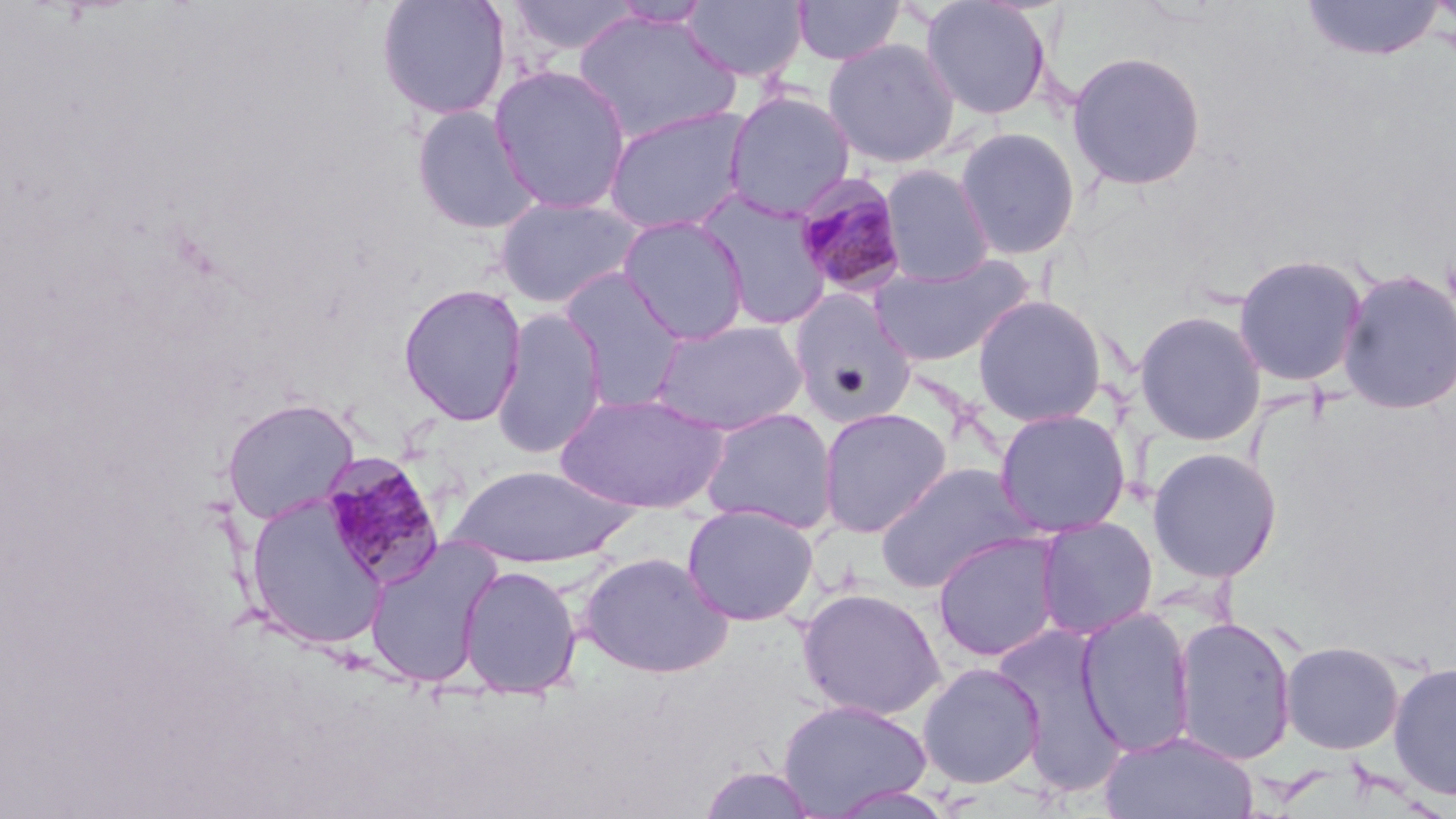

slide-level diagnosis = Plasmodium malariae
preparation = thin blood smear
magnification = 1000x
uninfected red blood cell locations = approximate bounding boxes as (x1, y1, x2, y2) in pixels: (375, 0, 510, 121), (505, 0, 644, 57), (792, 0, 906, 65), (918, 0, 1053, 121), (607, 1, 714, 29), (682, 1, 810, 84), (1300, 1, 1448, 62), (573, 10, 740, 146), (822, 37, 960, 169), (1067, 50, 1207, 191), (489, 64, 632, 214), (723, 90, 857, 219), (603, 105, 754, 235), (410, 106, 543, 235), (953, 126, 1082, 261), (879, 164, 996, 286), (694, 188, 835, 330), (493, 195, 645, 309), (616, 214, 751, 345), (868, 251, 1036, 367), (1233, 252, 1369, 387), (558, 267, 690, 412), (1337, 267, 1456, 415), (398, 283, 527, 426), (787, 290, 918, 426), (971, 293, 1109, 427), (490, 309, 609, 460), (1132, 309, 1267, 446), (648, 319, 810, 435), (554, 390, 729, 514), (221, 398, 359, 525), (817, 406, 952, 538), (698, 407, 840, 535), (993, 408, 1132, 538), (1146, 447, 1282, 583), (873, 462, 1036, 593), (446, 465, 637, 569), (245, 494, 387, 650), (681, 502, 820, 626), (1035, 515, 1158, 640), (932, 531, 1065, 662), (364, 537, 501, 688), (578, 551, 733, 679), (458, 565, 582, 697), (797, 587, 946, 720), (1077, 606, 1195, 756), (1172, 614, 1298, 765), (991, 622, 1129, 795), (1280, 640, 1405, 754), (1387, 661, 1456, 802), (916, 662, 1046, 789), (778, 697, 932, 817), (1100, 728, 1258, 818), (697, 766, 820, 818)
field of view = one of a larger specimen
modality = light microscopy
image size = 1456×819 pixels
Plasmodium malariae-infected red blood cell locations = approximate bounding boxes as (x1, y1, x2, y2) in pixels: (791, 172, 911, 300), (319, 454, 445, 589)
stain = May-Grünwald-Giemsa